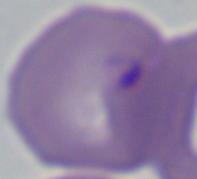
modality = micrograph
magnification = 1000x
identification = Babesia